State which parasite is depicted.
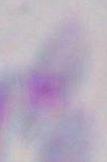
Toxoplasma gondii.

magnification = 1000x
modality = micrograph